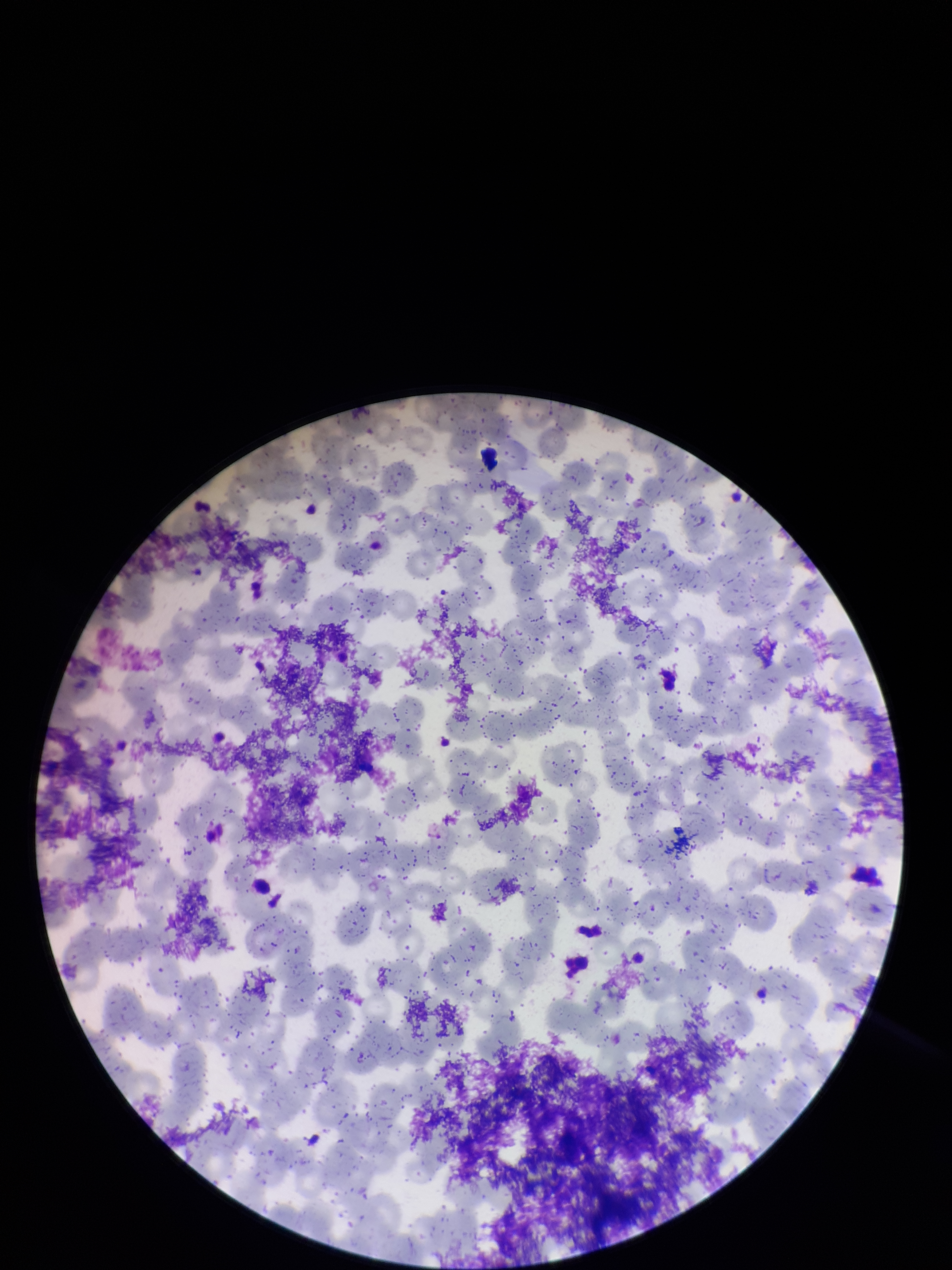 Parasitized red blood cells: none seen. Giemsa stain. Image is 952×1270 pixels. Parasitized red blood cell count: 0. One field from this slide. Red blood cell count: 309. Preparation: thin smear. Smartphone photograph taken through the eyepiece of a microscope. Patient malaria status: negative.